Assess the morphology of the erythrocytes.
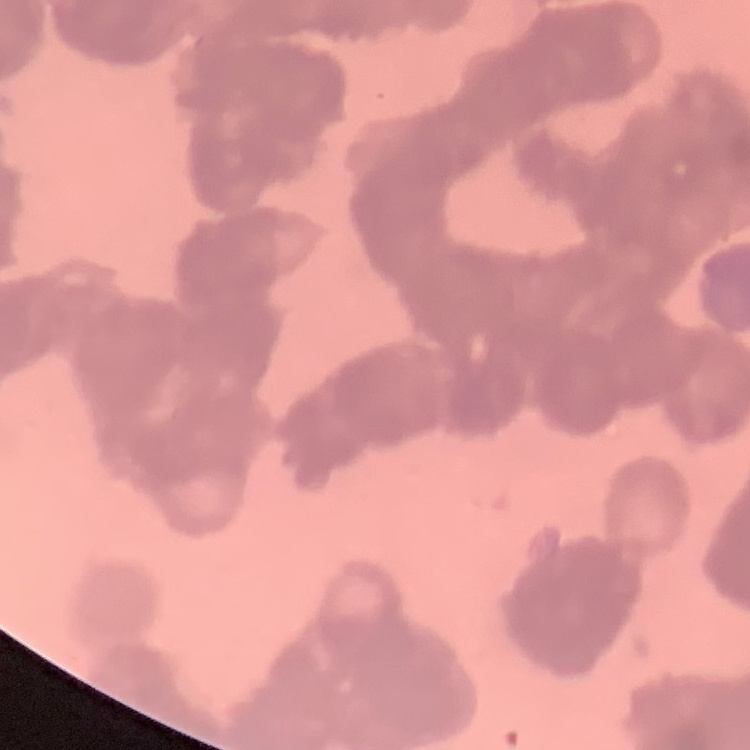

Rouleaux formation.

stain = Field's or Giemsa
image type = one tile cut from a larger photomicrograph
preparation = thin peripheral smear